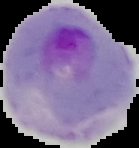

Summary:
  - Result: malaria parasites detected
  - Image size: 139×148 pixels
  - Preparation: thin blood film
  - Image type: segmented cell region on a black background